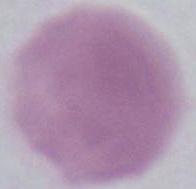

Summary:
  - Modality: photomicrograph
  - Identification: erythrocyte
  - Magnification: 1000x